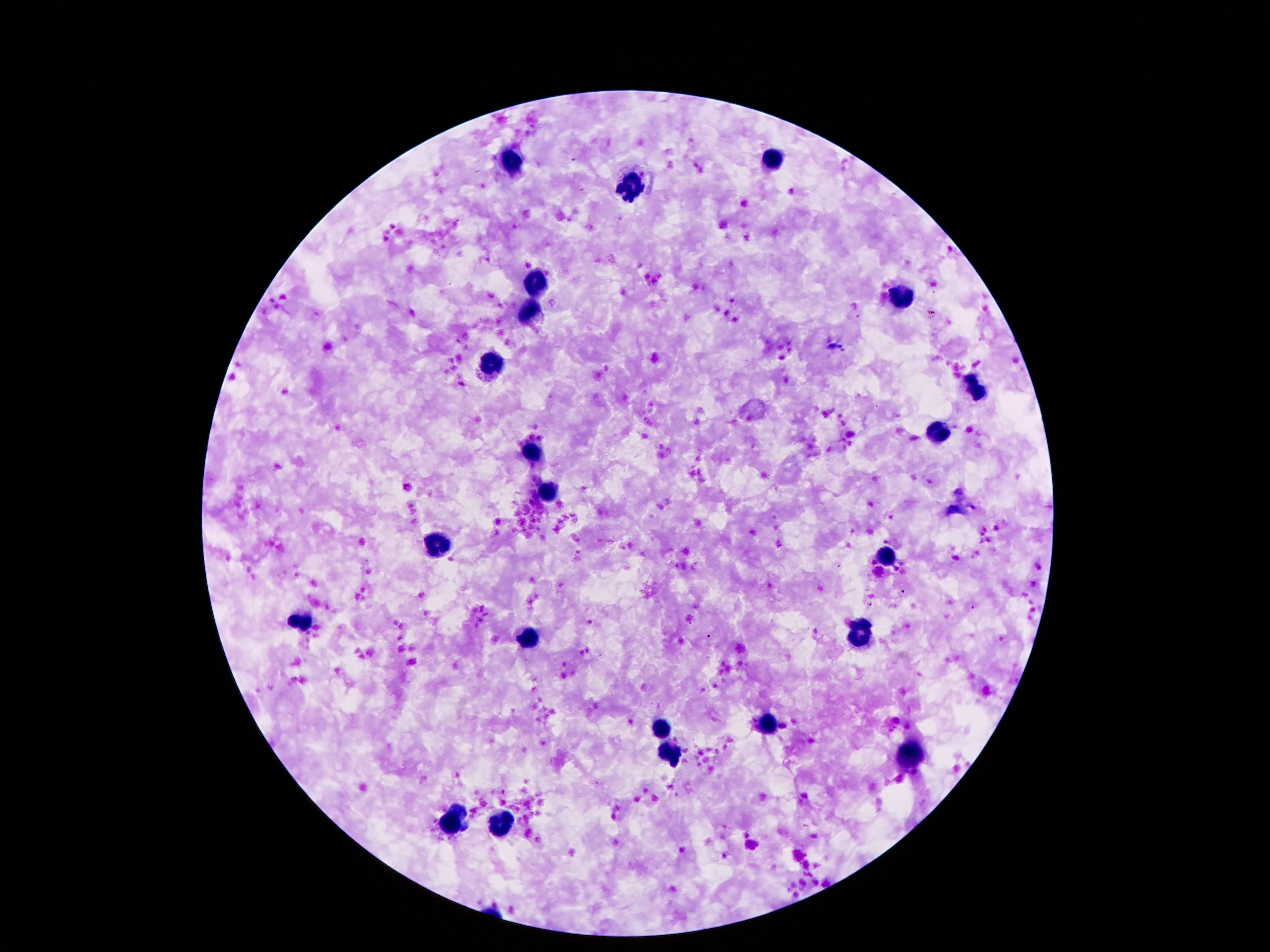
Approximate object centers, in pixels from the top-left corner. Leukocyte locations: (x=772, y=157), (x=511, y=160), (x=631, y=191), (x=536, y=281), (x=899, y=296), (x=529, y=313), (x=490, y=365), (x=976, y=391), (x=940, y=430), (x=529, y=455), (x=549, y=492), (x=438, y=545), (x=883, y=556), (x=302, y=623), (x=863, y=634), (x=529, y=638), (x=765, y=724), (x=658, y=728), (x=668, y=752), (x=915, y=754), (x=454, y=819), (x=502, y=822). Smartphone photograph taken through the microscope eyepiece. Patient malaria status: negative. Single field of view. Giemsa stain. Thick peripheral-blood smear. Image is 1270×952 pixels. 100x magnification.